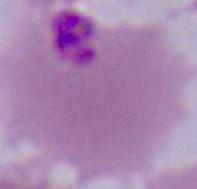
Captured at either 400x or 1000x magnification. A Plasmodium parasite is seen. Micrograph.